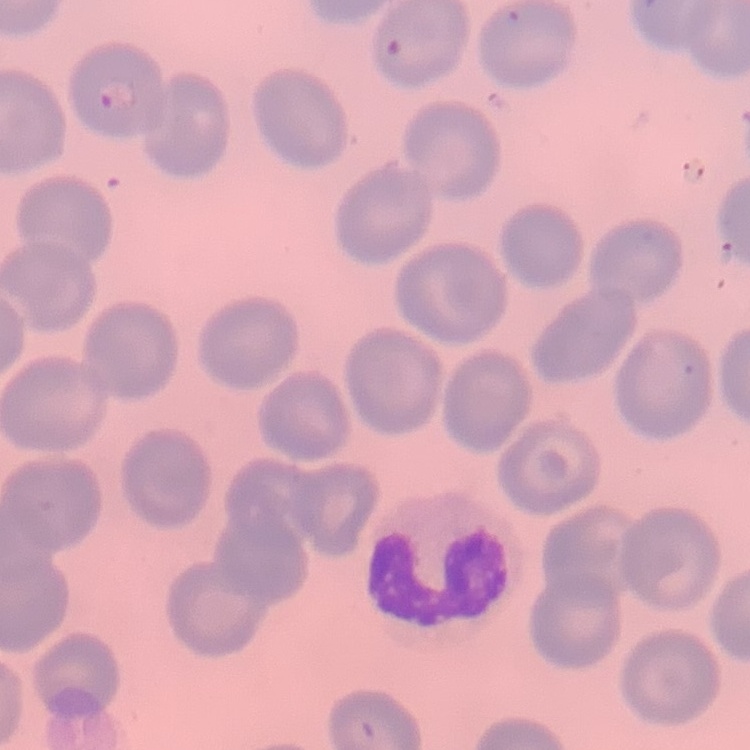

red blood cell morphology = no rouleaux formation
stain = Field's or Giemsa
preparation = thin blood smear
image type = one tile cut from a larger photomicrograph